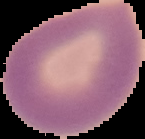

Image is 145×139 pixels. From a thin blood film. Malaria status: uninfected. The area outside the segmented cell region is set to black.